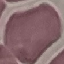

Summary:
  - Result: no malaria parasites seen
  - Stain: Giemsa
  - Capture: smartphone through the microscope eyepiece
  - Image type: automatically extracted cell patch, resized to 64 × 64 pixels
  - Preparation: thin blood film